Describe the morphology of the erythrocytes.
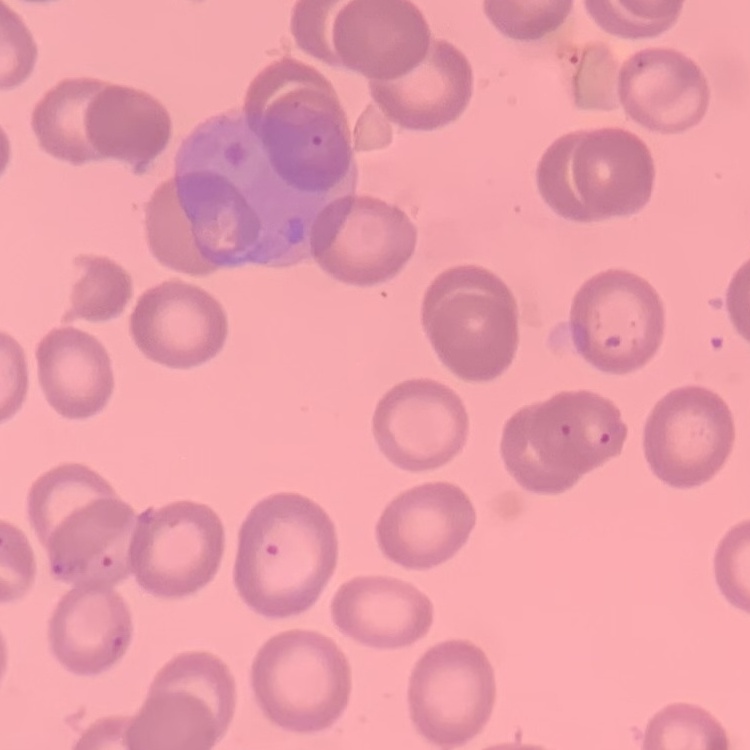

No rouleaux formation.

stain: Field's or Giemsa
image_type: square crop of a larger photomicrograph
preparation: thin peripheral smear